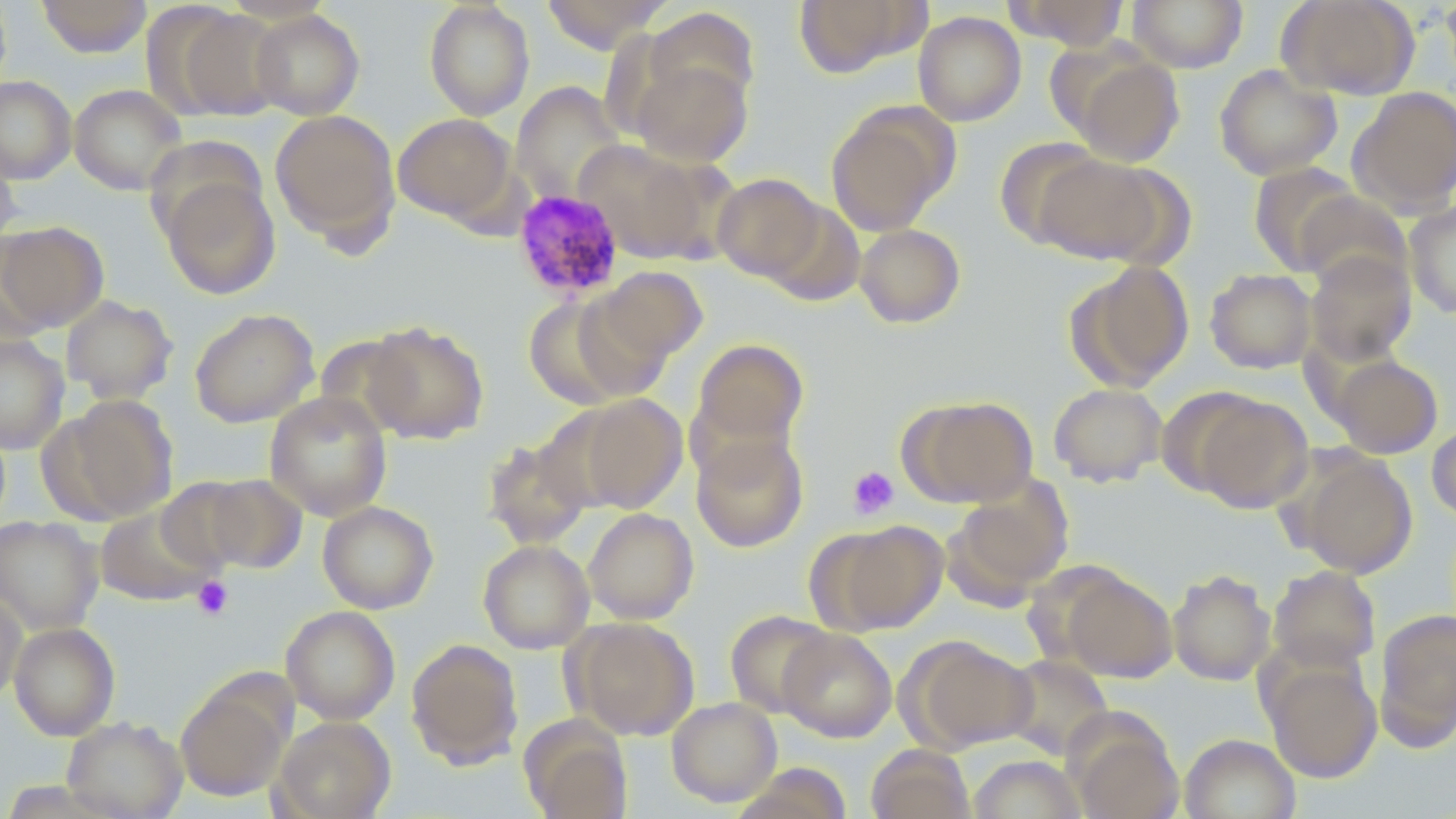

Approximate bounding boxes as named x1/y1/x2/y2 corners in pixels. Uninfected red blood cell locations: (x1=0, y1=0, x2=12, y2=99), (x1=37, y1=0, x2=152, y2=57), (x1=424, y1=0, x2=535, y2=120), (x1=540, y1=0, x2=671, y2=53), (x1=793, y1=0, x2=923, y2=78), (x1=1004, y1=0, x2=1130, y2=51), (x1=1128, y1=0, x2=1249, y2=73), (x1=1277, y1=0, x2=1420, y2=100), (x1=1439, y1=0, x2=1456, y2=90), (x1=166, y1=6, x2=286, y2=121), (x1=646, y1=8, x2=760, y2=115), (x1=249, y1=9, x2=365, y2=120), (x1=913, y1=11, x2=1026, y2=126), (x1=1062, y1=51, x2=1186, y2=167), (x1=629, y1=56, x2=754, y2=168), (x1=1214, y1=64, x2=1342, y2=180), (x1=0, y1=76, x2=77, y2=184), (x1=511, y1=82, x2=626, y2=206), (x1=69, y1=84, x2=187, y2=195), (x1=1348, y1=86, x2=1456, y2=215), (x1=825, y1=102, x2=956, y2=236), (x1=270, y1=109, x2=401, y2=249), (x1=393, y1=112, x2=516, y2=224), (x1=995, y1=137, x2=1108, y2=248), (x1=575, y1=141, x2=716, y2=262), (x1=0, y1=142, x2=22, y2=253), (x1=1035, y1=153, x2=1169, y2=266), (x1=1249, y1=162, x2=1363, y2=274), (x1=713, y1=173, x2=825, y2=282), (x1=160, y1=174, x2=281, y2=299), (x1=1299, y1=194, x2=1410, y2=292), (x1=1404, y1=201, x2=1456, y2=319), (x1=0, y1=221, x2=109, y2=332), (x1=855, y1=223, x2=966, y2=328), (x1=1305, y1=251, x2=1417, y2=366), (x1=1066, y1=260, x2=1194, y2=391), (x1=594, y1=265, x2=708, y2=367), (x1=1205, y1=268, x2=1317, y2=374), (x1=524, y1=294, x2=642, y2=407), (x1=60, y1=295, x2=178, y2=403), (x1=189, y1=308, x2=319, y2=428), (x1=362, y1=320, x2=489, y2=444), (x1=0, y1=334, x2=69, y2=454), (x1=692, y1=338, x2=809, y2=449), (x1=1330, y1=354, x2=1443, y2=458), (x1=1049, y1=382, x2=1167, y2=487), (x1=264, y1=391, x2=392, y2=521), (x1=1191, y1=393, x2=1313, y2=512), (x1=48, y1=394, x2=180, y2=523), (x1=573, y1=394, x2=686, y2=514), (x1=900, y1=394, x2=1038, y2=508), (x1=1427, y1=422, x2=1456, y2=521), (x1=691, y1=431, x2=809, y2=552), (x1=483, y1=436, x2=593, y2=549), (x1=1291, y1=451, x2=1417, y2=578), (x1=198, y1=473, x2=308, y2=574), (x1=157, y1=477, x2=261, y2=575), (x1=945, y1=479, x2=1074, y2=603), (x1=317, y1=501, x2=439, y2=614), (x1=95, y1=504, x2=217, y2=606), (x1=583, y1=508, x2=699, y2=624), (x1=0, y1=515, x2=103, y2=635), (x1=813, y1=519, x2=948, y2=634), (x1=477, y1=539, x2=594, y2=653), (x1=1268, y1=565, x2=1380, y2=673), (x1=1059, y1=567, x2=1178, y2=682), (x1=1167, y1=569, x2=1276, y2=686), (x1=0, y1=589, x2=27, y2=705), (x1=280, y1=605, x2=400, y2=724), (x1=1374, y1=608, x2=1456, y2=748), (x1=725, y1=610, x2=834, y2=718), (x1=568, y1=618, x2=700, y2=740), (x1=9, y1=622, x2=120, y2=740), (x1=778, y1=628, x2=897, y2=742), (x1=904, y1=636, x2=1034, y2=753), (x1=406, y1=638, x2=524, y2=769), (x1=1002, y1=654, x2=1113, y2=760), (x1=1263, y1=658, x2=1382, y2=782), (x1=175, y1=676, x2=292, y2=802), (x1=666, y1=696, x2=782, y2=806), (x1=1066, y1=714, x2=1184, y2=819), (x1=271, y1=715, x2=395, y2=819), (x1=62, y1=716, x2=188, y2=819), (x1=519, y1=716, x2=633, y2=819), (x1=1180, y1=733, x2=1301, y2=819), (x1=866, y1=744, x2=975, y2=819), (x1=968, y1=755, x2=1084, y2=818). Platelet locations: (x1=847, y1=466, x2=900, y2=520), (x1=192, y1=576, x2=234, y2=621). Plasmodium malariae-infected red blood cell locations: (x1=512, y1=189, x2=625, y2=300). Slide-level diagnosis: Plasmodium malariae. May-Grünwald-Giemsa-stained preparation. Captured at 1000x magnification. Light microscopy. Image is 1456×819 pixels. One field of a larger specimen. Thin blood smear.